Report the malaria status of this cell.
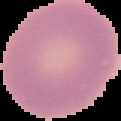

Uninfected.

From a thin blood film. Segmented cell region on a black background. Image is 121×121 pixels.